Report the malaria status of this cell.
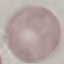

It is uninfected.

Summary:
  - Image type: automatically extracted cell patch, resized to 64 × 64 pixels
  - Stain: Giemsa
  - Capture: smartphone through the microscope eyepiece
  - Preparation: thin blood film